Assess this cell for malaria.
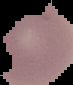
It is uninfected.

From a thin blood film. Cell region segmented out of the field of view; the surrounding area is masked to black. Image is 73×85 pixels.